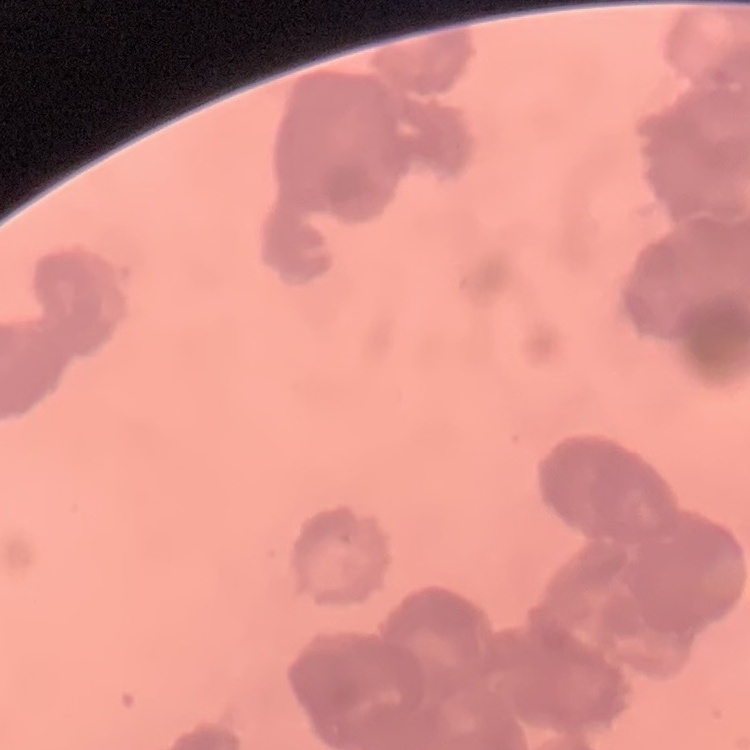 The red blood cells exhibit rouleaux formation. Field's or Giemsa stain. Thin peripheral smear. One tile cut from a larger photomicrograph.